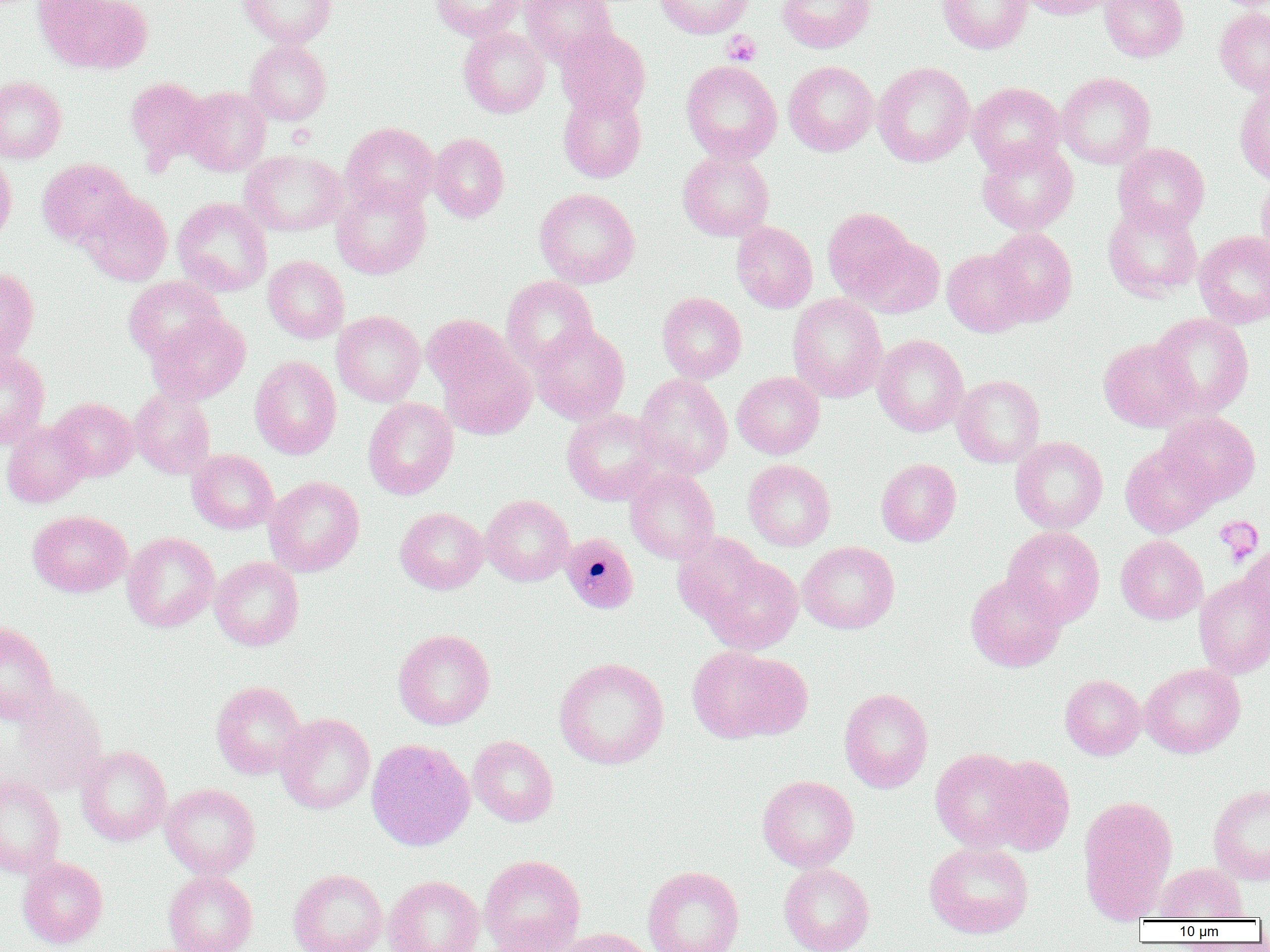

Approximate bounding boxes as (x1,y1)-(x2,y2) corner pairs in pixels. Plasmodium malariae-infected red blood cell locations: (561,532)-(639,614). Platelet locations: (722,30)-(760,66), (1214,516)-(1265,564). Uninfected red blood cell locations: (39,0)-(152,73), (239,0)-(338,47), (431,0)-(525,40), (521,0)-(616,64), (655,0)-(753,39), (777,0)-(875,52), (938,0)-(1032,53), (1021,0)-(1117,19), (1101,0)-(1188,61), (1214,7)-(1270,96), (459,27)-(549,118), (555,27)-(650,119), (245,39)-(332,125), (681,60)-(782,163), (784,61)-(878,156), (872,62)-(975,166), (1057,72)-(1155,169), (0,76)-(67,164), (125,76)-(212,169), (967,82)-(1066,174), (1235,82)-(1270,186), (182,86)-(271,176), (558,88)-(646,182), (341,122)-(439,213), (429,133)-(510,222), (976,139)-(1078,235), (1113,143)-(1210,234), (678,149)-(774,241), (240,150)-(347,236), (0,153)-(17,247), (37,158)-(135,247), (1256,175)-(1270,266), (331,180)-(431,279), (534,188)-(640,288), (78,190)-(173,286), (172,197)-(272,296), (1103,201)-(1202,301), (823,208)-(916,302), (732,221)-(818,313), (988,227)-(1077,325), (1194,230)-(1270,328), (852,235)-(944,318), (942,247)-(1031,337), (263,256)-(349,343), (0,266)-(39,363), (123,276)-(225,362), (501,276)-(598,371), (657,292)-(746,383), (787,293)-(887,402), (332,310)-(425,406), (147,312)-(250,404), (1150,313)-(1254,417), (421,314)-(516,398), (530,323)-(629,424), (872,334)-(968,436), (1099,337)-(1196,431), (439,348)-(536,440), (0,350)-(50,448), (250,356)-(341,459), (732,372)-(824,459), (634,373)-(733,479), (952,375)-(1045,467), (130,388)-(215,478), (50,397)-(138,480), (363,397)-(458,499), (562,409)-(663,505), (1159,411)-(1260,504), (1,420)-(90,507), (1010,436)-(1107,533), (1121,443)-(1217,537), (187,449)-(278,534), (876,458)-(961,546), (744,459)-(835,550), (625,468)-(720,563), (264,476)-(364,576), (481,494)-(574,586), (395,507)-(488,594), (28,510)-(132,597), (1003,526)-(1105,626), (121,531)-(220,632), (672,531)-(770,626), (1116,535)-(1207,624), (799,541)-(899,634), (1239,543)-(1269,631), (699,553)-(803,654), (210,556)-(304,650), (965,572)-(1067,672), (1194,574)-(1270,678), (0,622)-(58,724), (393,629)-(495,729), (686,645)-(809,743), (554,657)-(669,769), (1140,663)-(1245,757), (1060,674)-(1146,760), (210,680)-(307,779), (3,683)-(110,795), (839,687)-(933,792), (276,712)-(375,813), (468,736)-(558,826), (366,738)-(475,850), (76,745)-(172,845), (930,748)-(1031,852), (984,755)-(1075,855), (0,774)-(65,878), (758,775)-(858,872), (161,783)-(260,878), (1208,784)-(1270,885), (1078,795)-(1178,920), (924,842)-(1033,938), (480,855)-(585,952), (18,857)-(108,948), (778,863)-(874,952), (1154,863)-(1247,920), (642,865)-(744,952), (163,869)-(258,952), (288,869)-(388,952), (384,875)-(485,952), (480,927)-(585,952), (554,927)-(655,952). Slide-level diagnosis: Plasmodium malariae. Light microscopy. Single field of view. Thin blood smear. Image is 1270×952 pixels. Captured at 1000x magnification.